Outline each blood parasite and name the species.
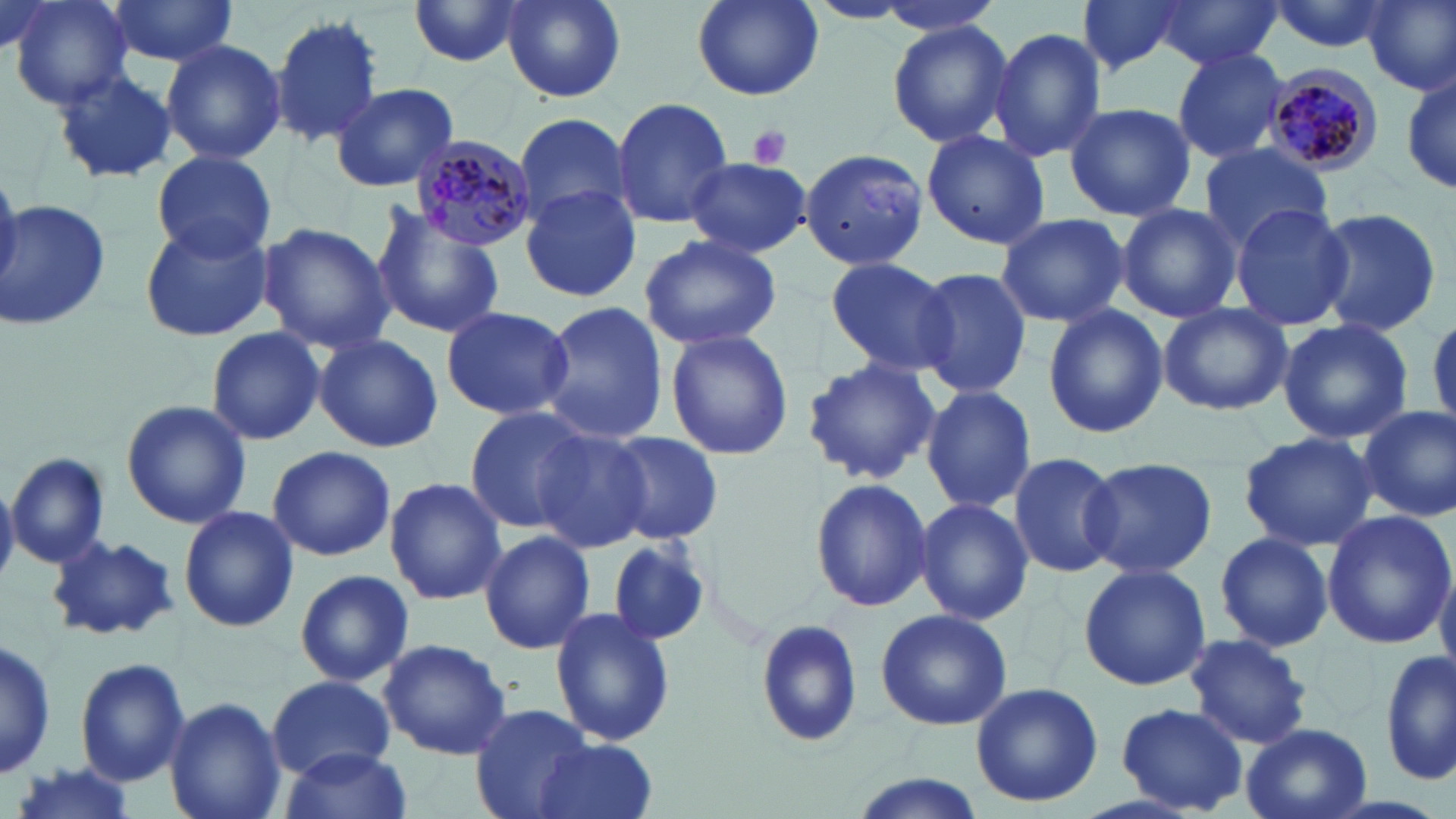
Approximate bounding boxes as (x1,y1)-(x2,y2) corner pairs in pixels.
Plasmodium malariae-infected red blood cells: (1262,67)-(1382,176), (408,133)-(537,251).
No Plasmodium falciparum, Plasmodium ovale, Plasmodium vivax, Babesia divergens, or Trypanosoma brucei observed.

{
  "slide_level_diagnosis": "Plasmodium malariae",
  "stain": "May-Grünwald-Giemsa",
  "magnification": "1000x",
  "platelet_locations": "approximate bounding boxes as (x1,y1)-(x2,y2) corner pairs in pixels: (747,125)-(792,168)",
  "field_of_view": "single",
  "modality": "optical microscopy",
  "image_size": "1456×819 pixels",
  "preparation": "thin blood smear",
  "uninfected_red_blood_cell_locations": "approximate bounding boxes as (x1,y1)-(x2,y2) corner pairs in pixels: (7,0)-(134,109), (106,0)-(239,68), (500,0)-(625,104), (690,0)-(826,102), (863,0)-(1009,37), (1076,0)-(1189,75), (1268,0)-(1395,55), (1363,0)-(1456,95), (405,1)-(531,69), (1156,2)-(1278,72), (271,14)-(384,148), (886,21)-(1014,147), (988,26)-(1107,163), (160,38)-(287,167), (1171,47)-(1287,163), (1399,65)-(1454,198), (51,67)-(178,185), (330,82)-(458,193), (612,96)-(734,229), (1063,102)-(1198,222), (513,113)-(633,225), (920,128)-(1052,249), (1197,144)-(1335,249), (798,148)-(929,271), (152,151)-(277,260), (685,156)-(811,257), (520,183)-(643,302), (4,197)-(111,330), (1116,203)-(1243,323), (1228,203)-(1353,331), (1311,206)-(1442,337), (370,207)-(507,340), (994,212)-(1131,328), (139,217)-(272,342), (258,223)-(394,354), (639,234)-(782,350), (824,257)-(957,378), (912,268)-(1031,397), (538,302)-(665,445), (1158,303)-(1292,415), (440,305)-(574,421), (1043,306)-(1169,438), (1278,318)-(1414,443), (204,326)-(326,446), (664,328)-(795,461), (315,335)-(443,452), (802,357)-(940,487), (920,385)-(1037,514), (121,399)-(254,529), (463,406)-(592,533), (1357,406)-(1455,522), (532,427)-(653,551), (603,431)-(724,544), (1239,431)-(1378,552), (267,445)-(396,562), (1008,451)-(1124,578), (6,452)-(110,568), (1083,457)-(1216,579), (808,476)-(932,614), (384,477)-(507,606), (0,478)-(19,587), (914,497)-(1033,625), (178,505)-(299,634), (1322,509)-(1455,650), (479,529)-(594,656), (1211,532)-(1336,651), (46,535)-(179,642), (606,535)-(715,646), (1436,560)-(1456,674), (1077,563)-(1210,689), (295,569)-(414,687), (550,606)-(675,746), (875,610)-(1015,731), (754,617)-(866,748), (1182,632)-(1314,750), (0,635)-(55,783), (376,638)-(512,759), (1381,647)-(1456,789), (75,658)-(190,787), (266,673)-(395,780), (970,681)-(1103,809), (165,697)-(286,819), (470,703)-(593,819), (1117,703)-(1250,814), (1241,723)-(1374,819), (531,737)-(658,819), (282,747)-(413,819), (9,764)-(142,819), (849,772)-(989,819)"
}